Describe the morphology of the erythrocytes.
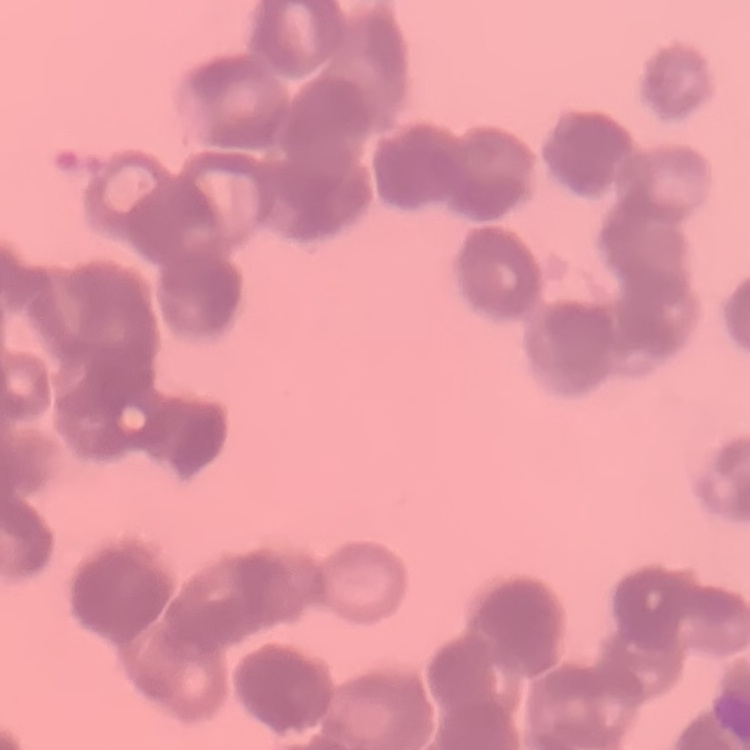

Rouleaux formation.

Summary:
  - Preparation: thin blood smear
  - Image type: one tile cut from a larger photomicrograph
  - Stain: Field's or Giemsa